Identify the preparation type.
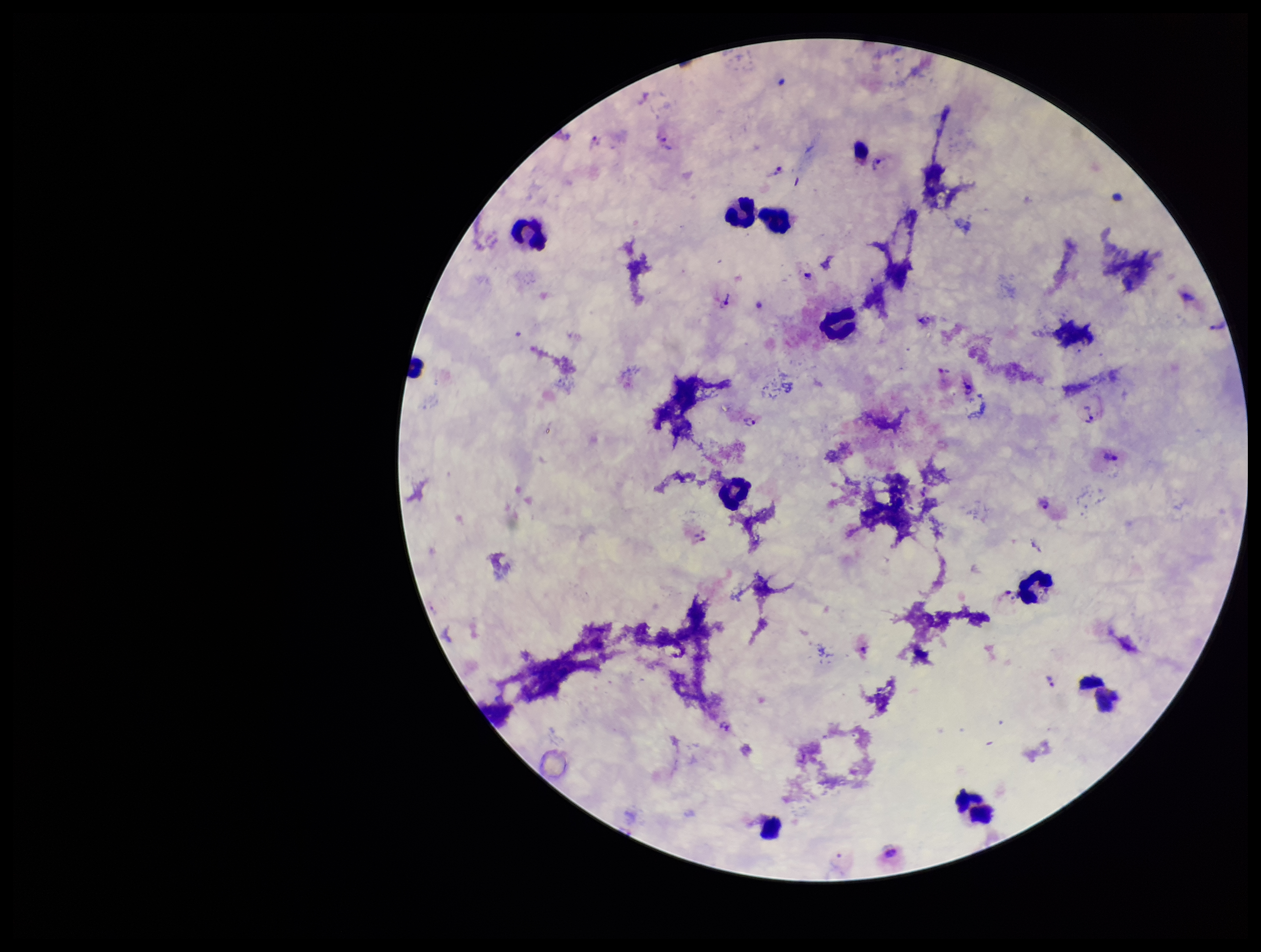

It is a thick blood smear.

Summary:
  - Leukocyte count: 10
  - Stain: Giemsa
  - Plasmodium parasites: detected
  - Patient malaria status: infected
  - Species reported for this patient: Plasmodium vivax
  - Field of view: one from this slide
  - Parasite count: 13
  - Image size: 1261×952 pixels
  - Capture: smartphone photograph through the microscope eyepiece